Assess the morphology of the erythrocytes.
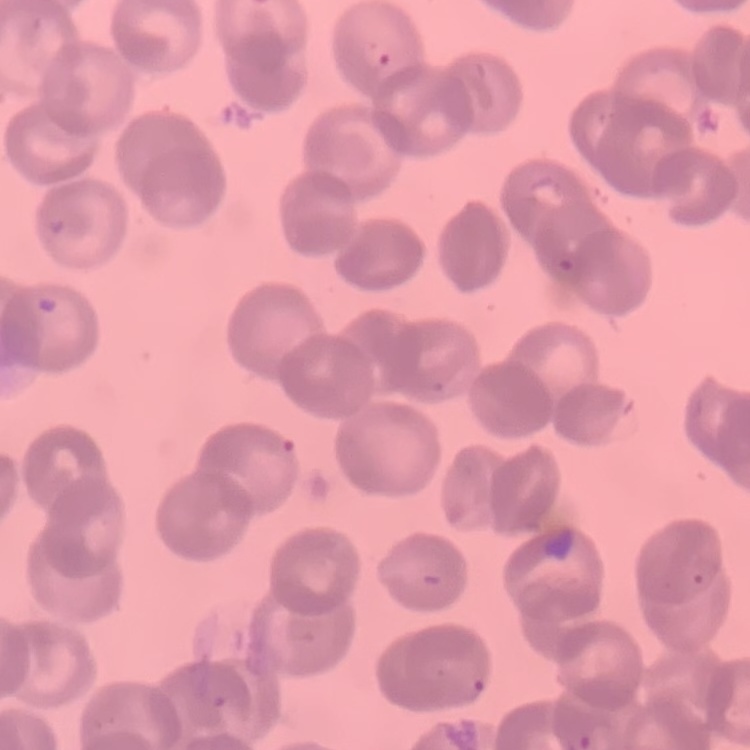

They show rouleaux formation.

Square crop of a larger photomicrograph. Field's or Giemsa stain. Thin blood smear.